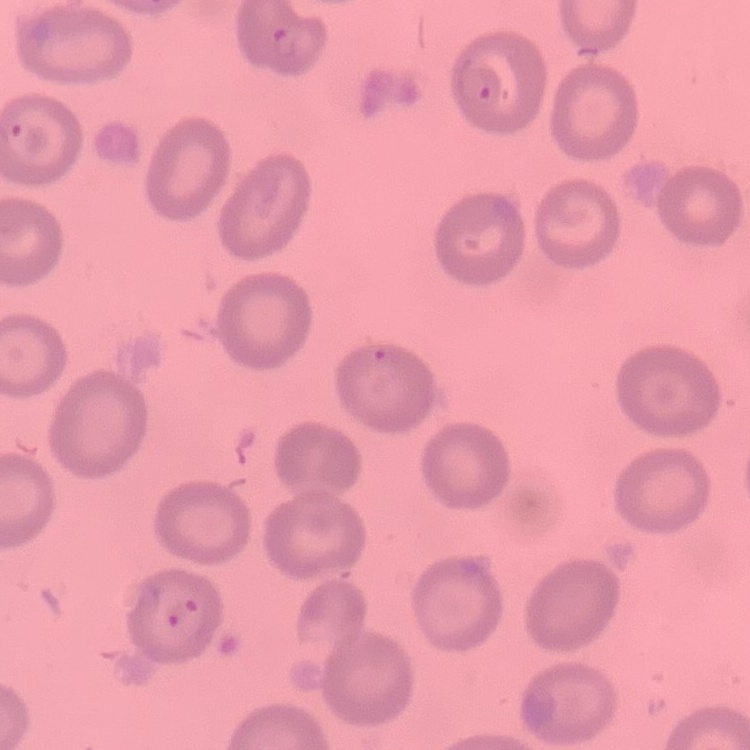 The erythrocytes show no rouleaux formation. Field's or Giemsa stain. One tile cut from a larger photomicrograph. Thin blood smear.